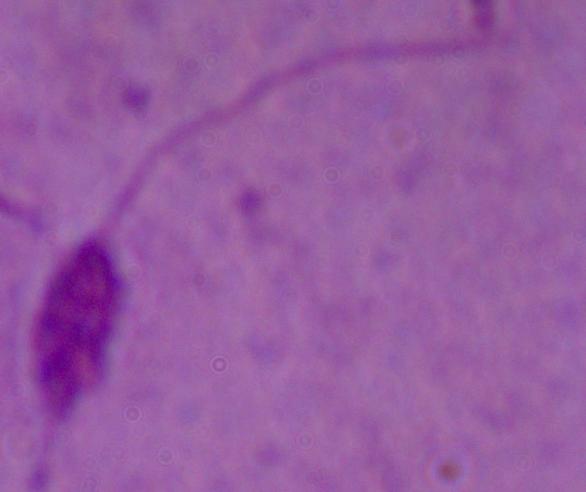
{
  "identification": "Leishmania",
  "magnification": "1000x",
  "modality": "micrograph"
}